Outline each Plasmodium vivax-infected red blood cell.
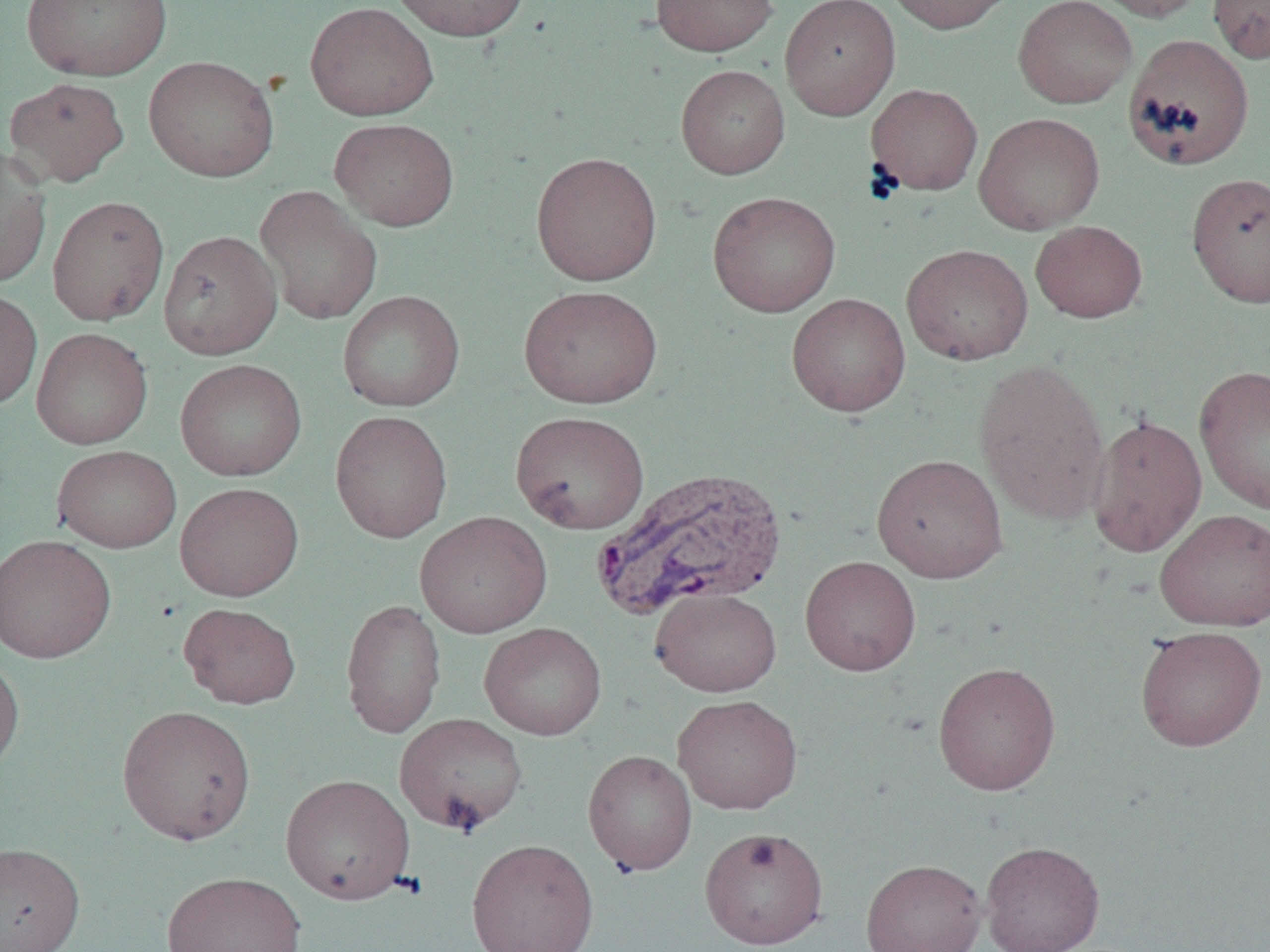
Approximate bounding boxes as named x1/y1/x2/y2 corners in pixels.
Plasmodium vivax-infected red blood cells: (x1=591, y1=465, x2=787, y2=620).

Summary:
  - Uninfected red blood cell locations: (x1=21, y1=0, x2=173, y2=81), (x1=389, y1=0, x2=531, y2=41), (x1=650, y1=0, x2=778, y2=57), (x1=780, y1=0, x2=900, y2=120), (x1=883, y1=0, x2=1016, y2=35), (x1=1013, y1=0, x2=1137, y2=108), (x1=1087, y1=0, x2=1208, y2=22), (x1=1208, y1=0, x2=1270, y2=63), (x1=305, y1=1, x2=438, y2=121), (x1=1122, y1=34, x2=1254, y2=171), (x1=143, y1=55, x2=279, y2=182), (x1=675, y1=64, x2=790, y2=179), (x1=4, y1=76, x2=129, y2=187), (x1=865, y1=83, x2=983, y2=196), (x1=973, y1=112, x2=1105, y2=235), (x1=329, y1=117, x2=459, y2=231), (x1=0, y1=145, x2=52, y2=290), (x1=531, y1=151, x2=662, y2=286), (x1=1187, y1=172, x2=1270, y2=308), (x1=254, y1=185, x2=382, y2=325), (x1=707, y1=191, x2=841, y2=318), (x1=47, y1=195, x2=170, y2=326), (x1=1030, y1=220, x2=1147, y2=322), (x1=158, y1=230, x2=283, y2=360), (x1=901, y1=244, x2=1033, y2=366), (x1=518, y1=284, x2=662, y2=409), (x1=0, y1=288, x2=43, y2=410), (x1=337, y1=290, x2=466, y2=412), (x1=786, y1=293, x2=910, y2=416), (x1=31, y1=327, x2=153, y2=449), (x1=973, y1=357, x2=1110, y2=525), (x1=175, y1=358, x2=307, y2=481), (x1=1193, y1=364, x2=1270, y2=517), (x1=330, y1=410, x2=453, y2=543), (x1=510, y1=410, x2=650, y2=534), (x1=1086, y1=413, x2=1207, y2=558), (x1=51, y1=444, x2=182, y2=553), (x1=871, y1=453, x2=1008, y2=584), (x1=174, y1=481, x2=304, y2=601), (x1=1154, y1=508, x2=1270, y2=631), (x1=414, y1=511, x2=552, y2=638), (x1=0, y1=533, x2=116, y2=664), (x1=800, y1=555, x2=921, y2=676), (x1=649, y1=587, x2=781, y2=697), (x1=340, y1=599, x2=446, y2=738), (x1=178, y1=602, x2=301, y2=709), (x1=479, y1=622, x2=607, y2=741), (x1=1135, y1=626, x2=1267, y2=751), (x1=0, y1=653, x2=25, y2=776), (x1=932, y1=661, x2=1061, y2=795), (x1=672, y1=694, x2=803, y2=815), (x1=117, y1=705, x2=256, y2=845), (x1=394, y1=712, x2=528, y2=835), (x1=582, y1=749, x2=697, y2=876), (x1=280, y1=773, x2=416, y2=904), (x1=699, y1=826, x2=829, y2=949), (x1=466, y1=838, x2=599, y2=952), (x1=980, y1=840, x2=1105, y2=952), (x1=0, y1=842, x2=86, y2=952), (x1=861, y1=859, x2=986, y2=952), (x1=161, y1=871, x2=307, y2=952)
  - Slide-level diagnosis: Plasmodium vivax
  - Preparation: thin blood smear
  - Modality: optical microscopy
  - Field of view: single
  - Image size: 1270×952 pixels
  - Magnification: 1000x